State the blood parasite species.
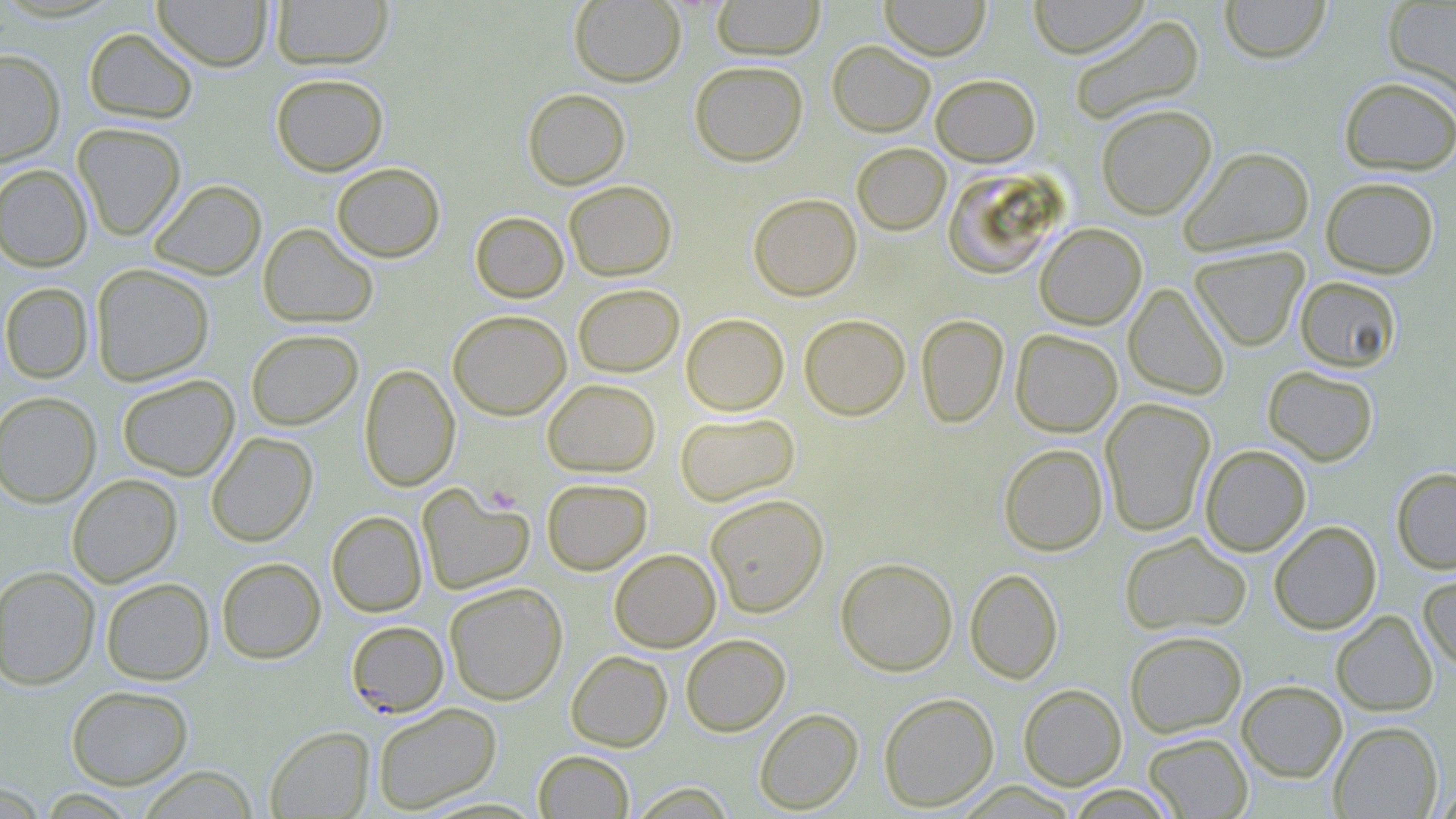

Plasmodium falciparum.

image_size: 1456×819 pixels
modality: optical microscopy
stain: May-Grünwald-Giemsa
field_of_view: single
plasmodium_falciparum_infected_red_blood_cell_locations: 'approximate bounding boxes as named x1/y1/x2/y2 corners in pixels: (x1=346, y1=621, x2=449, y2=717)'
preparation: thin blood film
platelet_locations: 'approximate bounding boxes as named x1/y1/x2/y2 corners in pixels: (x1=484, y1=483, x2=521, y2=514)'
magnification: 1000x
uninfected_red_blood_cell_locations: 'approximate bounding boxes as named x1/y1/x2/y2 corners in pixels: (x1=152, y1=0, x2=273, y2=71), (x1=270, y1=0, x2=394, y2=70), (x1=569, y1=0, x2=686, y2=87), (x1=711, y1=0, x2=825, y2=60), (x1=879, y1=0, x2=991, y2=60), (x1=1028, y1=0, x2=1149, y2=58), (x1=1219, y1=0, x2=1331, y2=63), (x1=1383, y1=0, x2=1456, y2=101), (x1=1068, y1=14, x2=1204, y2=125), (x1=83, y1=27, x2=198, y2=124), (x1=827, y1=40, x2=935, y2=137), (x1=0, y1=49, x2=65, y2=167), (x1=689, y1=60, x2=808, y2=166), (x1=270, y1=72, x2=389, y2=176), (x1=931, y1=74, x2=1040, y2=166), (x1=1339, y1=76, x2=1455, y2=176), (x1=523, y1=88, x2=630, y2=190), (x1=1096, y1=103, x2=1217, y2=219), (x1=72, y1=122, x2=186, y2=240), (x1=852, y1=142, x2=950, y2=235), (x1=1178, y1=145, x2=1314, y2=256), (x1=332, y1=162, x2=445, y2=262), (x1=0, y1=164, x2=93, y2=272), (x1=942, y1=167, x2=1062, y2=279), (x1=1320, y1=176, x2=1439, y2=279), (x1=148, y1=179, x2=266, y2=280), (x1=564, y1=180, x2=677, y2=281), (x1=748, y1=193, x2=862, y2=301), (x1=470, y1=211, x2=569, y2=303), (x1=1034, y1=222, x2=1147, y2=329), (x1=258, y1=223, x2=378, y2=328), (x1=1190, y1=246, x2=1309, y2=352), (x1=90, y1=264, x2=214, y2=385), (x1=1294, y1=275, x2=1402, y2=373), (x1=0, y1=282, x2=93, y2=383), (x1=573, y1=283, x2=684, y2=377), (x1=1124, y1=283, x2=1230, y2=400), (x1=447, y1=309, x2=571, y2=420), (x1=680, y1=313, x2=789, y2=416), (x1=799, y1=313, x2=910, y2=420), (x1=916, y1=313, x2=1009, y2=428), (x1=245, y1=329, x2=363, y2=431), (x1=1010, y1=329, x2=1122, y2=437), (x1=359, y1=364, x2=460, y2=491), (x1=1263, y1=365, x2=1379, y2=466), (x1=116, y1=374, x2=239, y2=481), (x1=542, y1=378, x2=660, y2=476), (x1=0, y1=391, x2=102, y2=508), (x1=1100, y1=398, x2=1216, y2=536), (x1=675, y1=411, x2=800, y2=506), (x1=206, y1=431, x2=318, y2=546), (x1=999, y1=443, x2=1108, y2=556), (x1=1200, y1=444, x2=1311, y2=556), (x1=1391, y1=468, x2=1456, y2=574), (x1=66, y1=474, x2=182, y2=587), (x1=542, y1=478, x2=652, y2=574), (x1=417, y1=484, x2=535, y2=595), (x1=706, y1=494, x2=829, y2=617), (x1=326, y1=511, x2=427, y2=617), (x1=1268, y1=521, x2=1382, y2=634), (x1=1120, y1=532, x2=1252, y2=636), (x1=609, y1=548, x2=720, y2=652), (x1=216, y1=557, x2=326, y2=664), (x1=835, y1=557, x2=958, y2=676), (x1=0, y1=566, x2=100, y2=690), (x1=965, y1=568, x2=1063, y2=683), (x1=1418, y1=571, x2=1456, y2=671), (x1=100, y1=577, x2=214, y2=685), (x1=444, y1=581, x2=567, y2=705), (x1=1331, y1=610, x2=1438, y2=716), (x1=1124, y1=630, x2=1247, y2=737), (x1=680, y1=633, x2=791, y2=736), (x1=566, y1=650, x2=673, y2=751), (x1=1236, y1=680, x2=1347, y2=782), (x1=1018, y1=683, x2=1127, y2=790), (x1=66, y1=685, x2=193, y2=789), (x1=878, y1=693, x2=999, y2=812), (x1=373, y1=702, x2=502, y2=813), (x1=754, y1=707, x2=863, y2=814), (x1=1329, y1=721, x2=1443, y2=818), (x1=265, y1=725, x2=375, y2=818), (x1=1143, y1=732, x2=1253, y2=818), (x1=533, y1=750, x2=634, y2=818), (x1=137, y1=765, x2=258, y2=818), (x1=628, y1=782, x2=737, y2=818)'